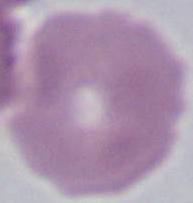

Summary:
  - Magnification: 1000x
  - Identification: red blood cell
  - Modality: micrograph